Classify this cell by malaria status.
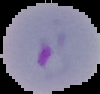

Parasitized.

Summary:
  - Image type: segmented cell region on a black background
  - Image size: 100×94 pixels
  - Preparation: thin blood film